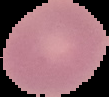

From a thin blood film. The area outside the segmented cell region is set to black. Result: no malaria parasites seen. Image is 109×97 pixels.